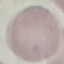
{
  "malaria_status": "uninfected",
  "preparation": "thin blood smear",
  "stain": "Giemsa",
  "image_type": "cell patch, automatically extracted from a larger field of view and resized to 64 × 64 pixels",
  "capture": "smartphone camera at the microscope eyepiece"
}